Describe the morphology of the red blood cells.
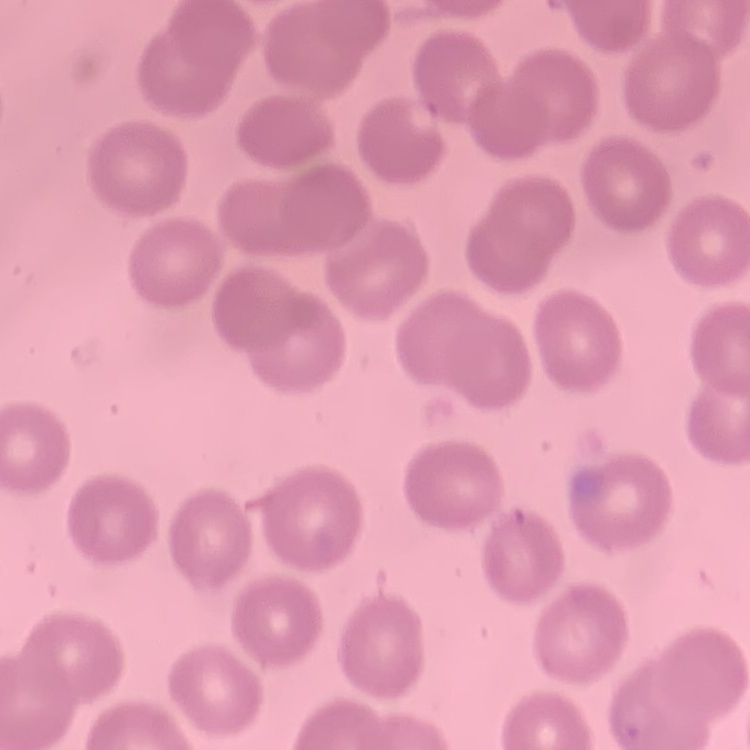
They show no rouleaux formation.

Summary:
  - Preparation: thin blood film
  - Stain: Field's or Giemsa
  - Image type: one tile cut from a larger photomicrograph